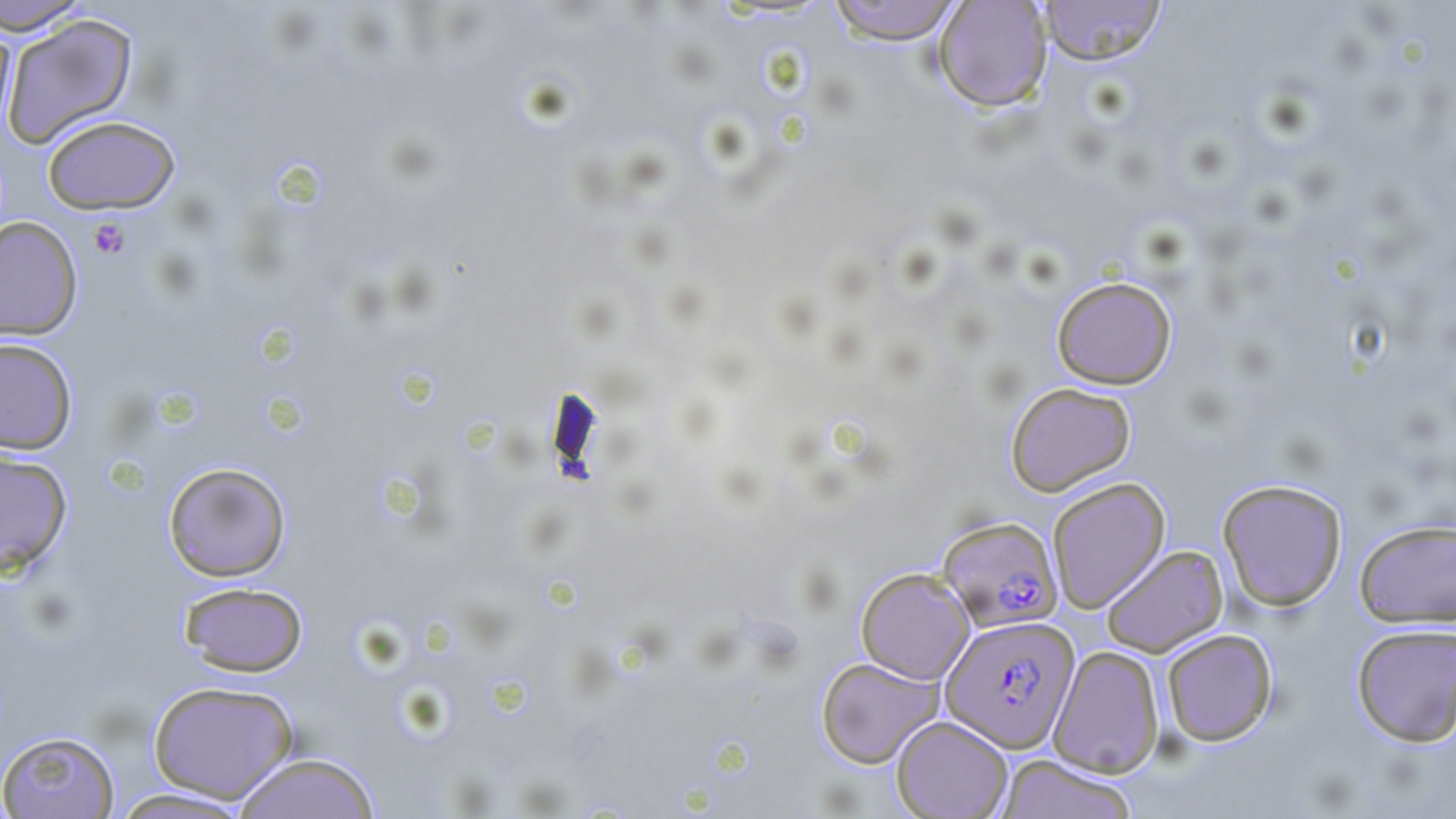

{
  "slide_level_diagnosis": "Plasmodium falciparum",
  "platelet_locations": "approximate bounding boxes as (x1, y1, x2, y2) in pixels: (88, 217, 131, 260)",
  "uninfected_red_blood_cell_locations": "approximate bounding boxes as (x1, y1, x2, y2) in pixels: (0, 0, 94, 37), (826, 0, 965, 45), (933, 0, 1053, 112), (1038, 0, 1166, 65), (1, 12, 139, 148), (0, 18, 17, 138), (42, 115, 180, 215), (0, 217, 83, 340), (1051, 275, 1177, 390), (0, 337, 78, 454), (1005, 381, 1136, 496), (0, 448, 73, 577), (163, 462, 292, 581), (1047, 477, 1170, 612), (1217, 478, 1348, 611), (1354, 519, 1456, 628), (1100, 544, 1228, 657), (855, 567, 975, 684), (178, 581, 309, 677), (1351, 624, 1456, 746), (1161, 628, 1278, 746), (1049, 646, 1164, 778), (816, 656, 943, 769), (147, 679, 299, 804), (891, 715, 1013, 818), (0, 730, 121, 818), (232, 752, 381, 819), (996, 754, 1140, 819), (108, 787, 256, 818)",
  "field_of_view": "one of a larger specimen",
  "stain": "May-Grünwald-Giemsa",
  "preparation": "thin blood smear",
  "modality": "optical microscopy",
  "image_size": "1456×819 pixels",
  "magnification": "1000x",
  "plasmodium_falciparum_infected_red_blood_cell_locations": "approximate bounding boxes as (x1, y1, x2, y2) in pixels: (936, 515, 1063, 633), (940, 614, 1080, 753)"
}